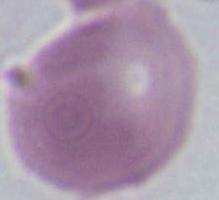
Summary:
  - Modality: photomicrograph
  - Magnification: 1000x
  - Identification: red blood cell